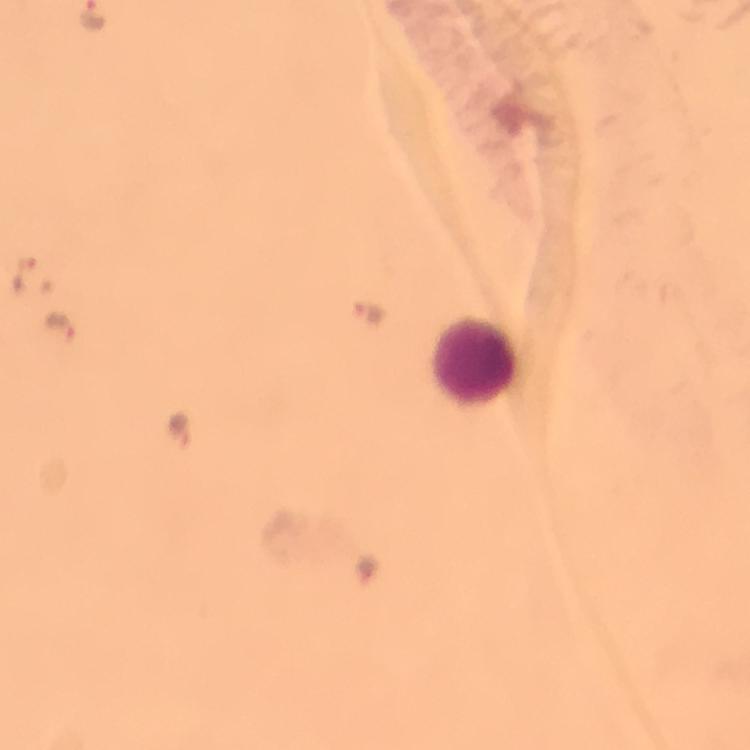
Approximate object centers, in pixels from the top-left corner.
Summary:
  - Leukocyte locations: (x=476, y=365)
  - Malaria parasite locations: (x=26, y=277), (x=370, y=313), (x=63, y=327), (x=181, y=426)
  - Preparation: thick smear
  - Capture: smartphone mounted on the microscope
  - Image size: 750×750 pixels
  - Stain: Giemsa
  - Cropped from: one field of view
  - Immersion oil: used
  - Magnification: 100x
  - Context: from a malaria diagnostic workup